Assess the morphology of the red blood cells.
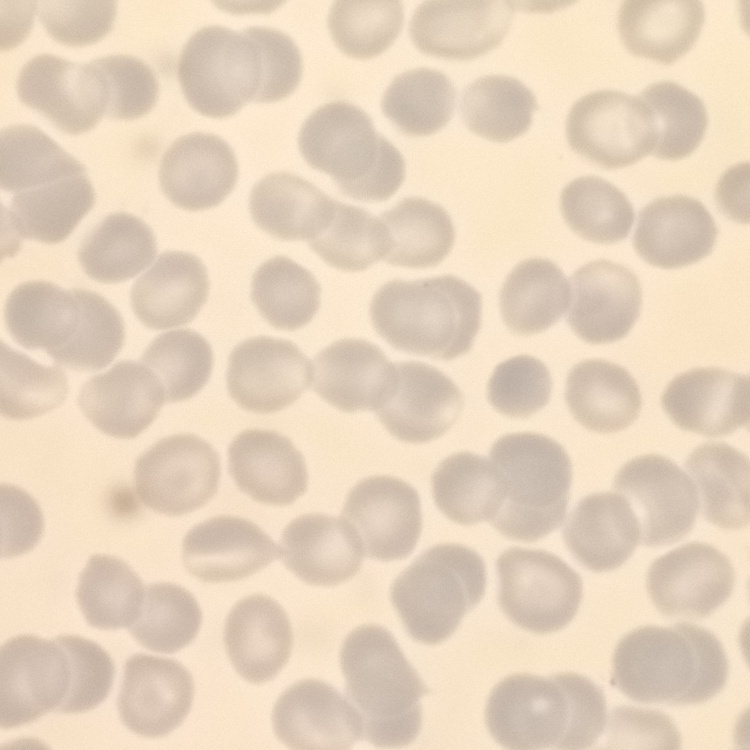

They show no rouleaux formation.

Stained with either Field's or Giemsa. Square crop of a larger photomicrograph. Thin blood smear.